Identify the blood parasite species.
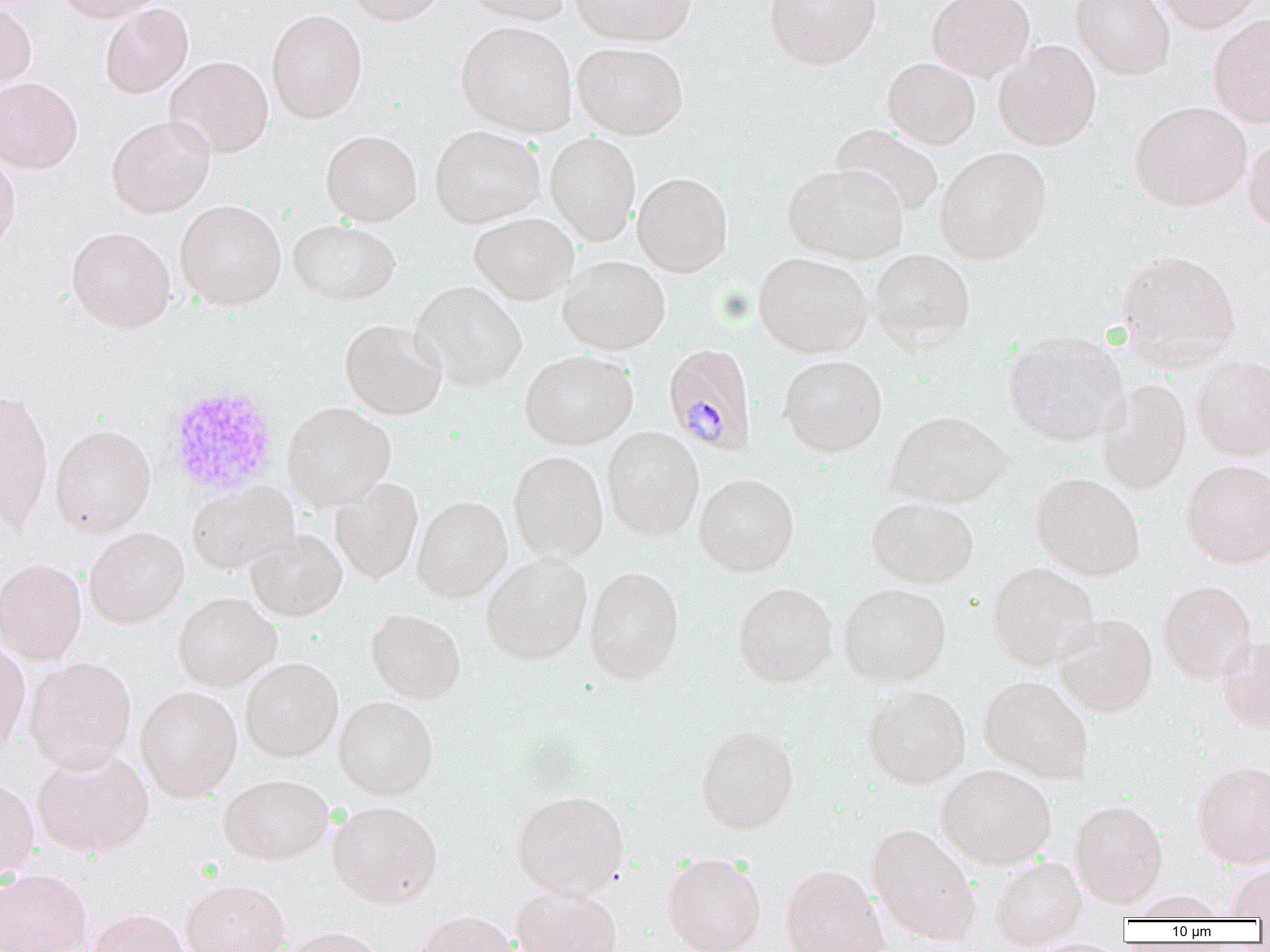
Plasmodium malariae.

modality = light microscopy
Plasmodium malariae-infected red blood cell locations = approximate bounding boxes as (x1, y1, x2, y2) in pixels: (663, 343, 757, 455)
uninfected red blood cell locations = approximate bounding boxes as (x1, y1, x2, y2) in pixels: (53, 0, 164, 23), (345, 0, 448, 25), (457, 0, 569, 24), (569, 0, 697, 46), (765, 0, 881, 69), (927, 0, 1035, 82), (1070, 0, 1175, 80), (1153, 0, 1266, 33), (0, 2, 36, 93), (99, 3, 194, 99), (266, 9, 367, 124), (1208, 13, 1270, 127), (456, 20, 577, 137), (993, 40, 1101, 150), (573, 41, 688, 140), (164, 56, 273, 158), (883, 57, 980, 148), (0, 77, 83, 173), (1130, 101, 1252, 210), (106, 115, 215, 218), (830, 123, 945, 218), (430, 125, 545, 227), (321, 130, 422, 226), (545, 132, 641, 245), (1242, 134, 1270, 232), (935, 147, 1052, 264), (0, 150, 21, 252), (783, 163, 908, 263), (632, 172, 733, 276), (175, 200, 286, 310), (469, 213, 578, 304), (287, 218, 400, 305), (66, 226, 177, 333), (869, 248, 975, 353), (1115, 249, 1242, 369), (753, 252, 872, 357), (558, 255, 670, 355), (411, 281, 527, 391), (340, 318, 447, 419), (1004, 330, 1126, 445), (519, 349, 638, 450), (779, 354, 887, 457), (1192, 355, 1270, 460), (1096, 379, 1192, 493), (0, 389, 54, 533), (282, 402, 396, 511), (886, 409, 1013, 509), (50, 423, 156, 536), (602, 426, 704, 542), (508, 451, 608, 563), (1182, 459, 1270, 568), (1031, 472, 1146, 580), (694, 473, 799, 576), (330, 477, 423, 583), (187, 481, 297, 574), (412, 495, 512, 602), (866, 497, 979, 588), (84, 527, 189, 628), (245, 529, 347, 621), (480, 554, 591, 665), (0, 557, 87, 665), (988, 562, 1099, 670), (584, 565, 684, 684), (1158, 579, 1257, 683), (733, 582, 838, 688), (838, 583, 951, 686), (173, 592, 281, 691), (366, 608, 465, 703), (1054, 613, 1158, 717), (1218, 633, 1270, 734), (0, 637, 31, 756), (24, 656, 137, 773), (239, 657, 343, 761), (979, 675, 1095, 783), (862, 685, 971, 788), (135, 686, 242, 801), (334, 696, 438, 799), (695, 724, 800, 834), (31, 745, 154, 858), (1192, 759, 1270, 867), (936, 763, 1057, 869), (219, 774, 333, 864), (0, 777, 40, 883), (510, 789, 629, 900), (1069, 798, 1168, 908), (327, 800, 443, 907), (865, 822, 982, 945), (662, 851, 767, 952), (988, 855, 1088, 948), (1227, 862, 1270, 919), (780, 863, 889, 952), (0, 868, 93, 952), (180, 878, 290, 952), (511, 886, 623, 952), (1125, 890, 1230, 922), (88, 907, 192, 952), (413, 909, 520, 952), (280, 925, 389, 952)
image size = 1270×952 pixels
magnification = 1000x
field of view = single
preparation = thin blood film
platelet locations = approximate bounding boxes as (x1, y1, x2, y2) in pixels: (165, 384, 281, 499)